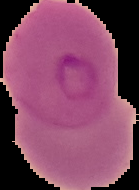
Malaria status: parasitized. From a thin blood smear. Image is 139×190 pixels. Cell region segmented out of the field of view; the surrounding area is masked to black.